Assess this cell for malaria.
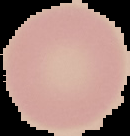
Uninfected.

Summary:
  - Image size: 130×136 pixels
  - Preparation: thin blood film
  - Image type: segmented cell region on a black background